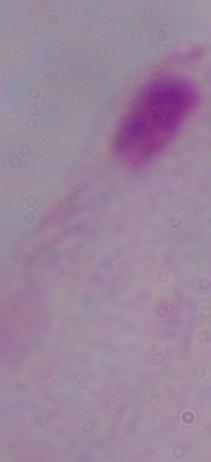

Summary:
  - Magnification: 1000x
  - Modality: photomicrograph
  - Identification: trichomonad